Assess this cell for malaria.
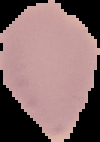
It is uninfected.

preparation = thin blood film
image size = 100×142 pixels
image type = segmented cell region with the area outside set to black